Give the extent of all uninfected red blood cells.
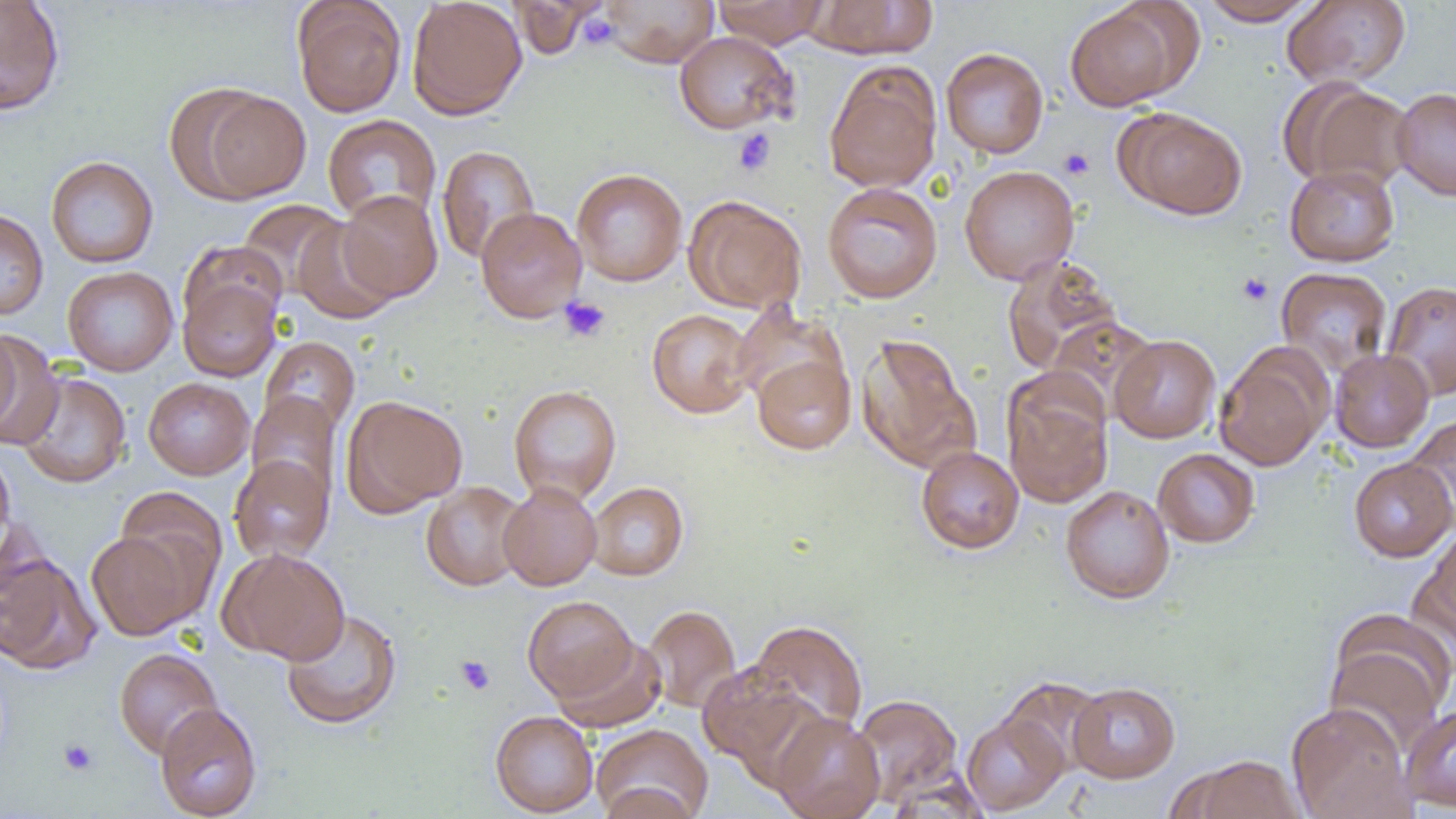
Approximate bounding boxes as (x1,y1)-(x2,y2) corner pairs in pixels.
Uninfected red blood cells: (292,0)-(406,117), (407,0)-(527,120), (601,0)-(718,66), (712,0)-(829,48), (805,0)-(938,58), (1198,0)-(1321,25), (1282,0)-(1411,88), (0,1)-(65,115), (507,1)-(602,58), (1064,2)-(1190,111), (674,31)-(797,134), (941,48)-(1049,159), (823,61)-(943,193), (1284,79)-(1414,193), (1392,87)-(1456,201), (191,89)-(312,202), (1117,108)-(1248,219), (323,114)-(441,226), (436,145)-(541,264), (45,155)-(159,268), (1284,163)-(1400,267), (959,165)-(1080,285), (571,168)-(688,286), (822,182)-(943,304), (337,190)-(443,302), (684,195)-(807,314), (238,199)-(347,298), (475,206)-(587,322), (0,208)-(49,320), (291,218)-(399,325), (180,240)-(289,334), (1001,256)-(1124,375), (62,266)-(178,376), (1276,267)-(1393,377), (178,276)-(282,382), (1381,280)-(1456,401), (732,303)-(845,409), (646,309)-(758,418), (1046,316)-(1159,417), (0,326)-(22,440), (0,332)-(56,448), (856,334)-(978,473), (1109,334)-(1220,443), (259,337)-(360,437), (1215,345)-(1331,471), (1330,348)-(1434,452), (752,354)-(856,455), (17,371)-(131,489), (143,377)-(254,480), (1003,378)-(1113,509), (508,384)-(622,505), (247,392)-(341,504), (343,395)-(468,515), (1403,414)-(1456,527), (916,446)-(1024,554), (0,448)-(15,558), (1153,448)-(1260,547), (229,455)-(334,563), (1349,457)-(1455,562), (498,481)-(602,591), (586,481)-(689,581), (421,482)-(530,591), (1060,485)-(1175,604), (115,486)-(228,607), (1417,524)-(1456,645), (86,530)-(200,641), (219,548)-(350,665), (0,551)-(100,674), (522,595)-(637,703), (642,604)-(741,713), (281,608)-(402,730), (1324,610)-(1455,746), (748,619)-(868,735), (552,635)-(666,733), (114,648)-(223,760), (696,662)-(821,778), (1068,681)-(1180,783), (851,694)-(965,806), (155,702)-(262,818), (1286,702)-(1415,819), (1401,704)-(1456,812), (490,710)-(598,817), (961,711)-(1068,815), (770,712)-(885,819), (591,724)-(713,819), (1182,755)-(1305,819), (596,781)-(705,818).

slide-level diagnosis = no evidence of blood parasites
image size = 1456×819 pixels
field of view = single
preparation = thin blood film
platelet locations = approximate bounding boxes as (x1,y1)-(x2,y2) corner pairs in pixels: (579,13)-(619,50), (732,129)-(776,176), (1059,147)-(1095,180), (1237,272)-(1273,306), (559,296)-(612,343), (455,655)-(495,695), (58,738)-(99,776)
modality = optical microscopy
magnification = 1000x